Point out each Plasmodium parasite.
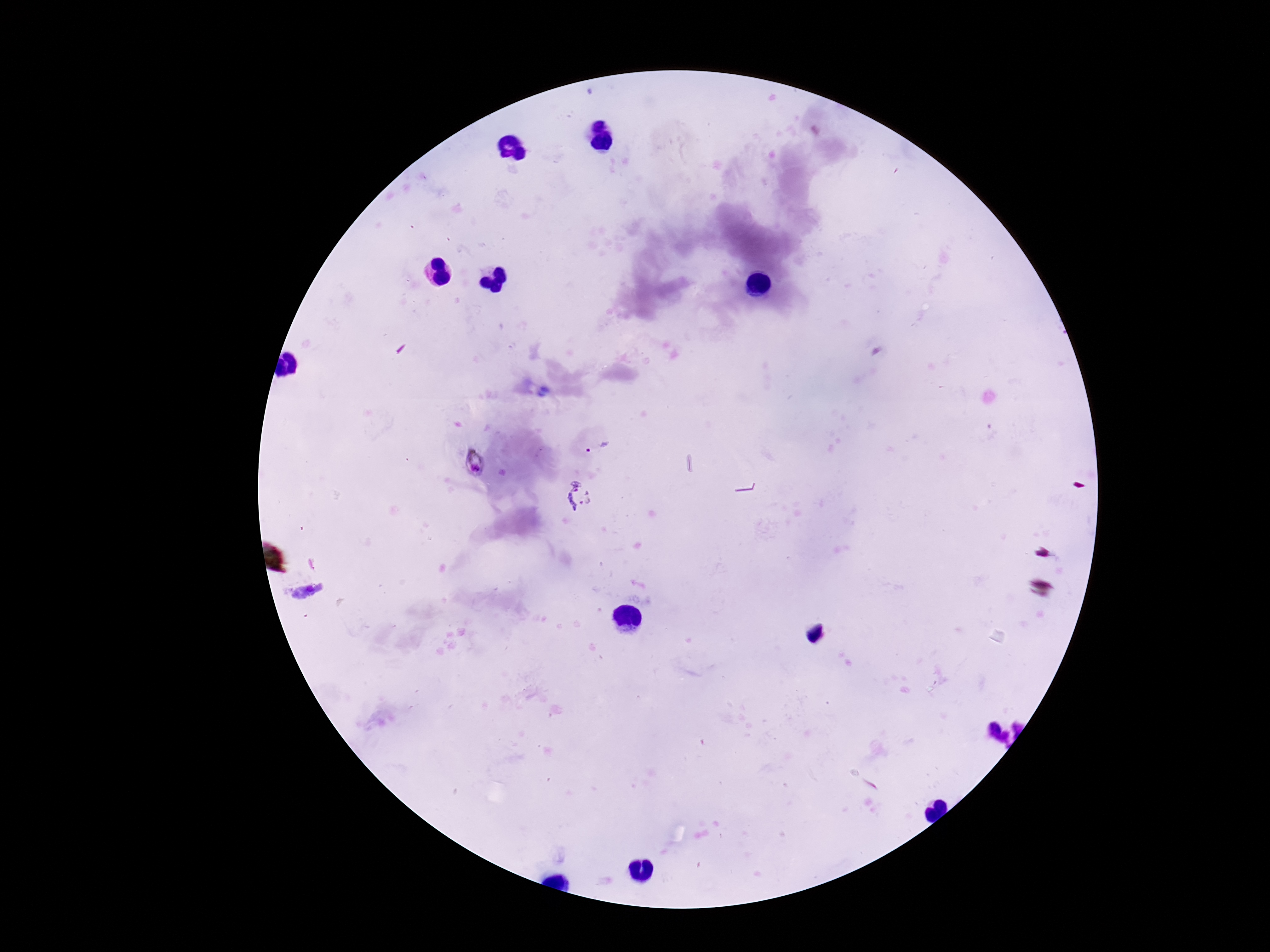

Approximate object centers, in pixels from the top-left corner.
Plasmodium parasites: (x=596, y=447), (x=581, y=496).

Summary:
  - Capture: smartphone camera through the microscope eyepiece
  - Magnification: 100x
  - Stain: Giemsa
  - Field of view: one from this slide
  - Preparation: thick peripheral-blood smear
  - Patient malaria status: infected
  - Image size: 1270×952 pixels